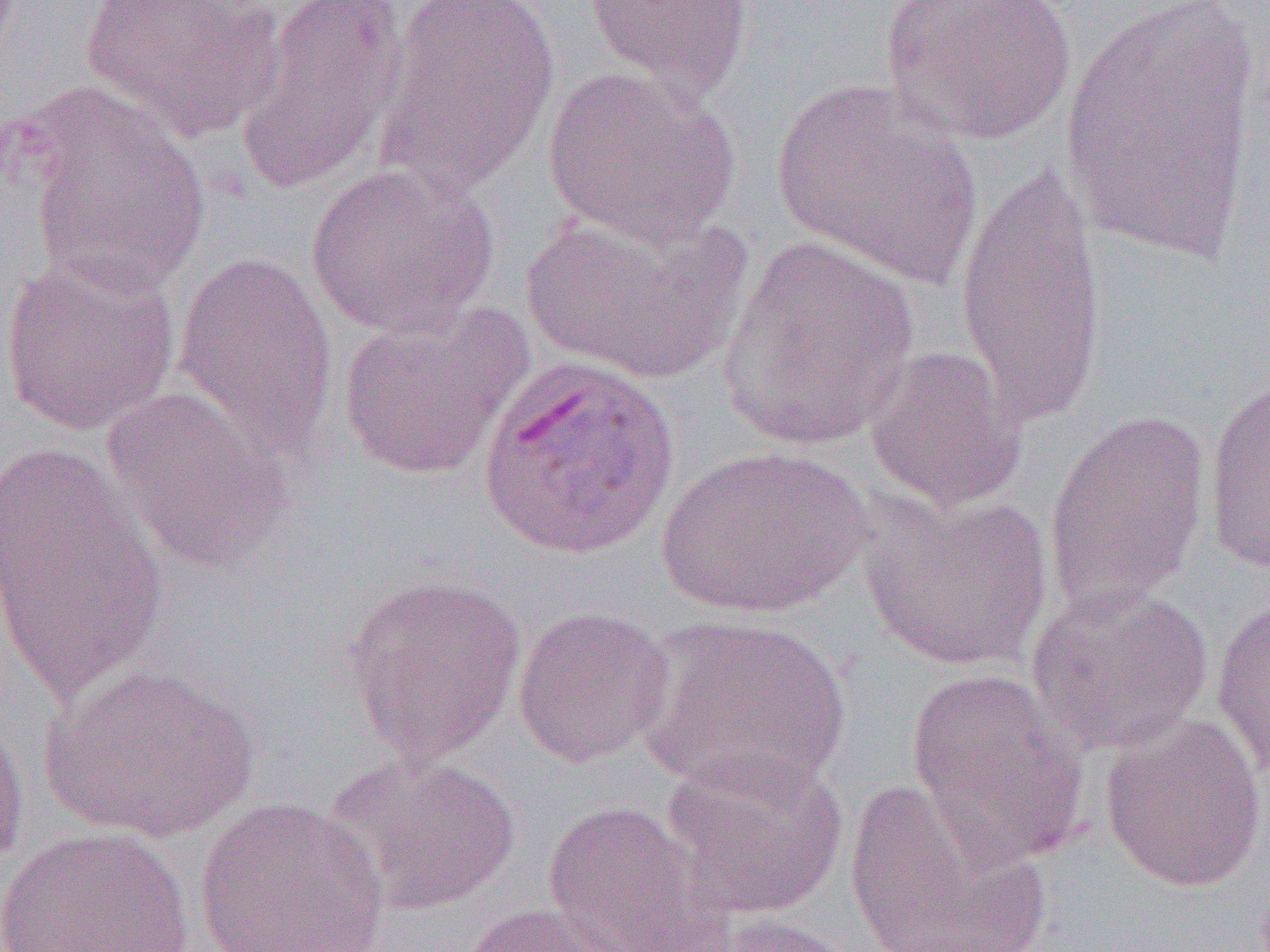
{
  "plasmodium_ovale_infected_red_blood_cell_locations": "approximate bounding boxes as (x1,y1)-(x2,y2) corner pairs in pixels: (474,353)-(683,563)",
  "slide_level_diagnosis": "Plasmodium ovale",
  "modality": "optical microscopy",
  "preparation": "thin blood smear",
  "image_size": "1270×952 pixels",
  "magnification": "1000x",
  "field_of_view": "single",
  "uninfected_red_blood_cell_locations": "approximate bounding boxes as (x1,y1)-(x2,y2) corner pairs in pixels: (83,0)-(285,141), (234,0)-(411,193), (373,0)-(560,193), (582,0)-(753,105), (879,0)-(1077,145), (1055,0)-(1266,268), (543,67)-(740,248), (771,80)-(981,289), (12,83)-(211,300), (955,159)-(1105,433), (305,163)-(500,338), (522,206)-(749,386), (717,237)-(922,451), (172,250)-(338,463), (1,251)-(181,436), (337,299)-(533,482), (863,344)-(1028,513), (1203,375)-(1269,575), (99,385)-(293,575), (1042,409)-(1212,617), (0,445)-(170,701), (655,445)-(871,619), (859,492)-(1052,672), (341,573)-(527,765), (1025,583)-(1214,755), (1211,590)-(1270,783), (512,605)-(674,768), (636,614)-(851,796), (39,660)-(262,843), (904,669)-(1089,869), (0,703)-(31,881), (1099,715)-(1267,892), (660,748)-(849,921), (326,753)-(519,914), (843,777)-(1050,952), (193,795)-(390,952), (541,800)-(730,952), (0,826)-(193,952), (460,901)-(648,952), (708,914)-(864,952)"
}